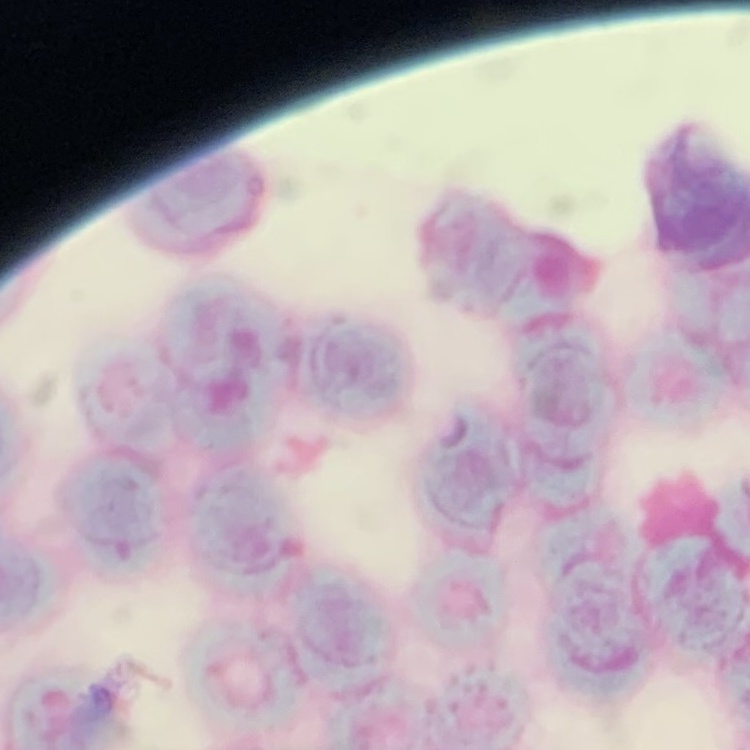

erythrocyte morphology = rouleaux formation
preparation = thin peripheral smear
image type = square crop of a larger photomicrograph
stain = Field's or Giemsa